Point out each Plasmodium parasite.
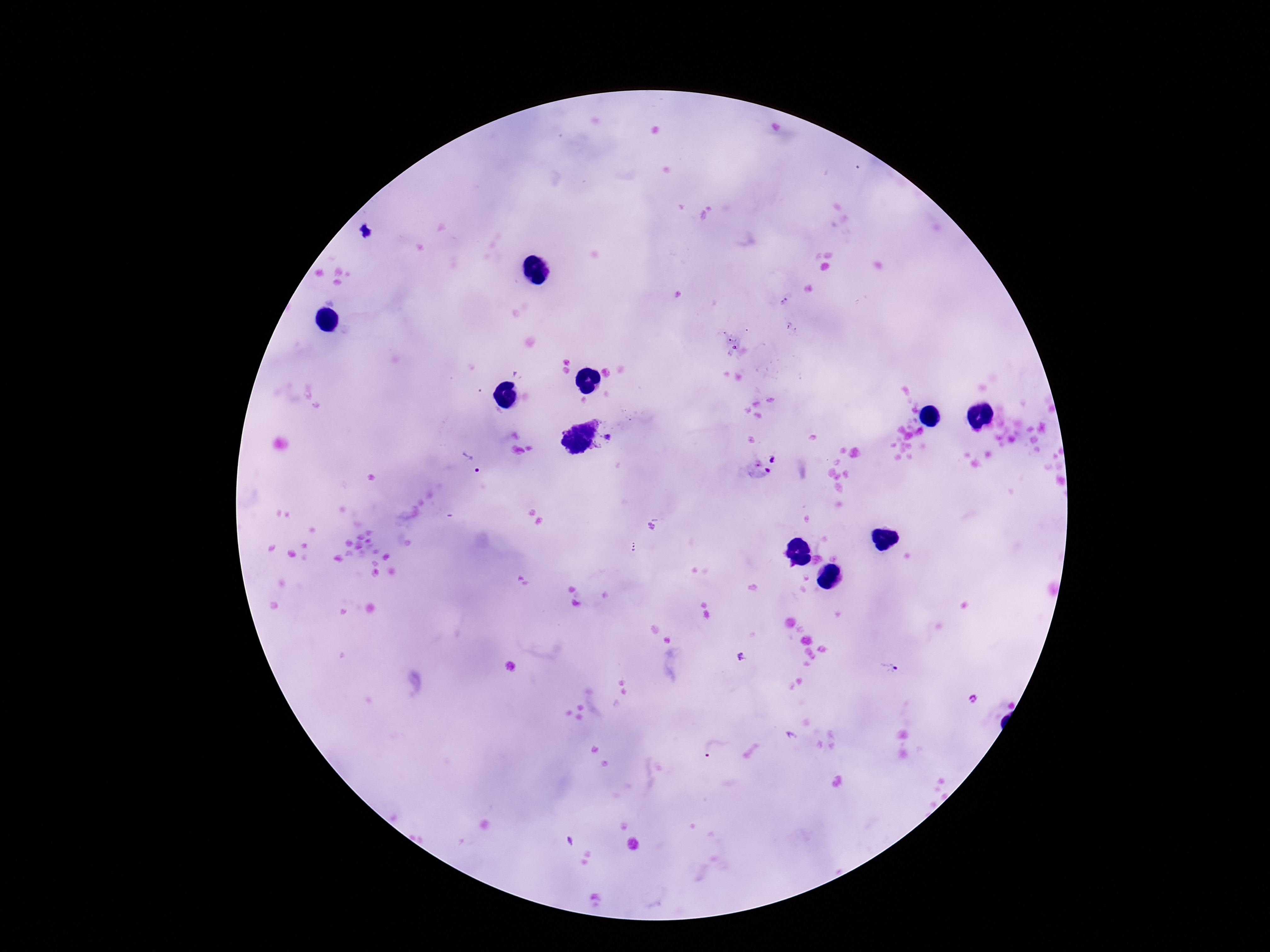
Approximate centers as (x, y) in pixels.
Plasmodium parasites: (785, 302), (789, 325), (729, 340), (734, 347), (608, 436), (574, 437), (774, 459), (471, 462), (759, 471), (634, 548), (741, 657), (889, 667), (973, 698), (712, 750), (571, 842).

magnification = 100x
image size = 1270×952 pixels
patient malaria status = positive
capture = smartphone camera through the microscope eyepiece
field of view = single
stain = Giemsa
preparation = thick peripheral-blood smear